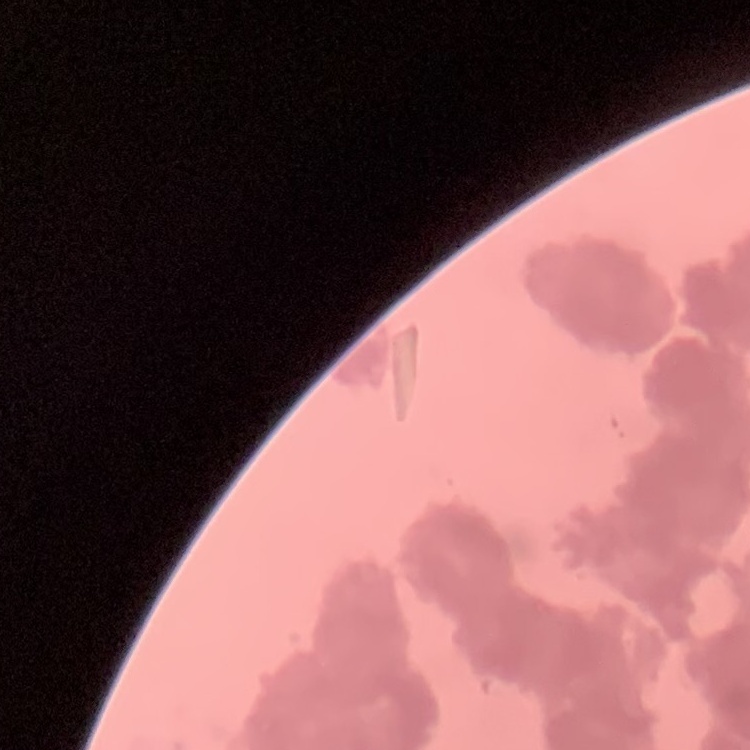

{
  "red_blood_cell_morphology": "rouleaux formation",
  "preparation": "thin peripheral smear",
  "image_type": "one tile cut from a larger photomicrograph",
  "stain": "Field's or Giemsa"
}